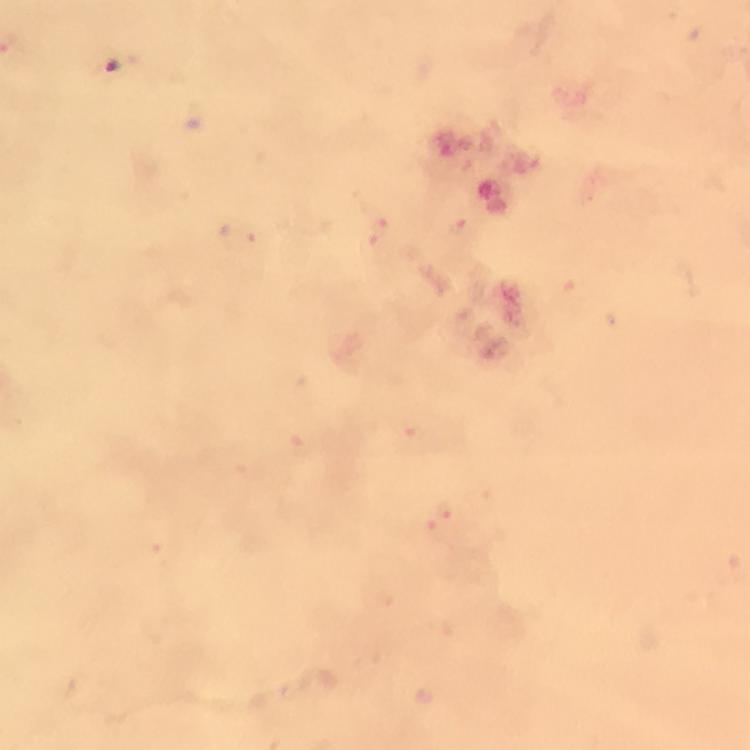

Approximate centers as (x, y) in pixels.
Summary:
  - Plasmodium parasite locations: (378, 226), (457, 228), (445, 514)
  - Cropped from: a single field of view
  - Stain: Giemsa
  - Magnification: 100x
  - Immersion oil: used
  - Capture: smartphone camera through the microscope
  - Context: from a diagnostic examination for malaria
  - Preparation: thick blood smear
  - Image size: 750×750 pixels